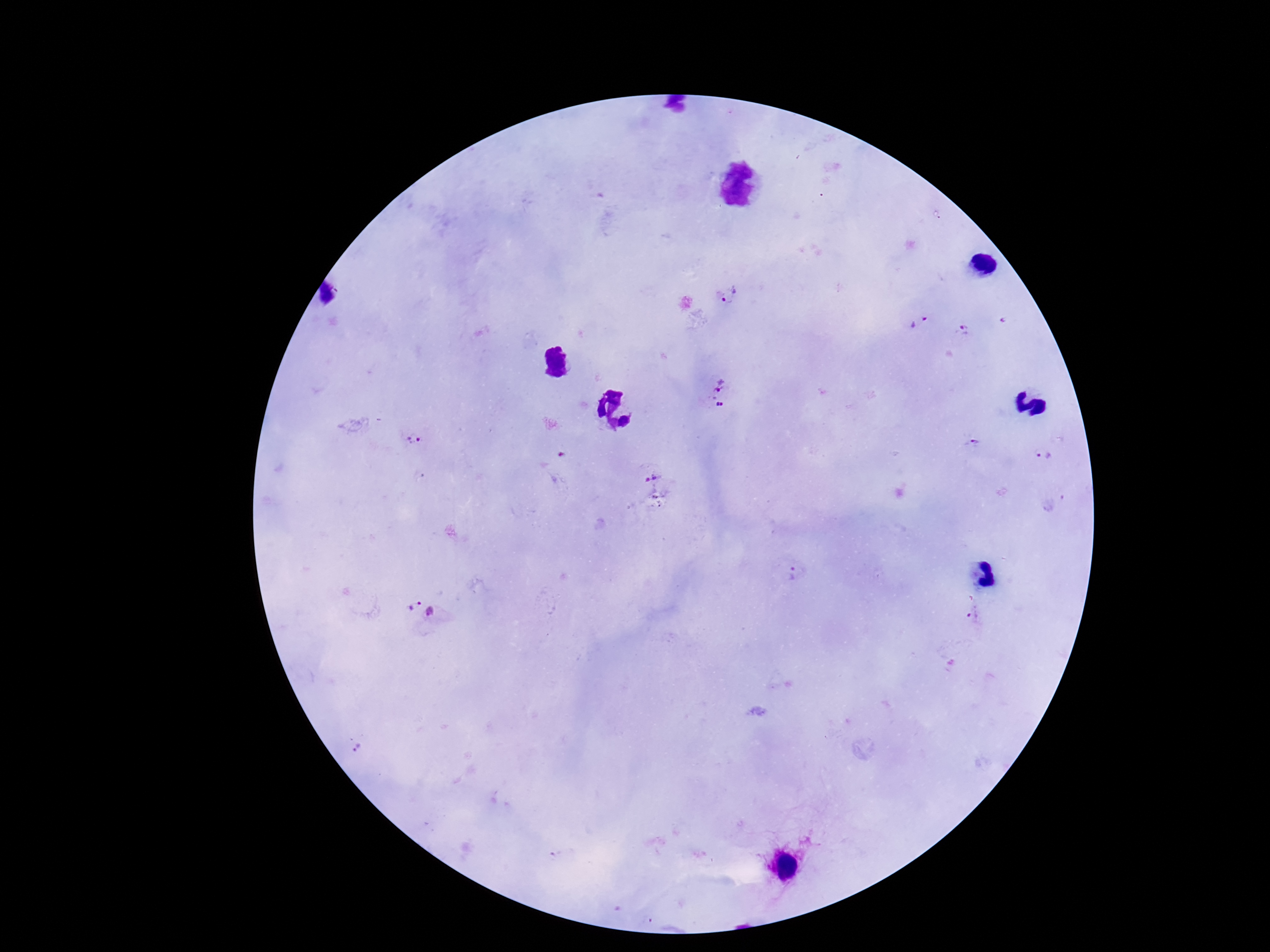

{
  "preparation": "thick peripheral-blood smear",
  "plasmodium_parasite_locations": "approximate centers as (x, y) in pixels: (730, 295), (918, 322), (964, 330), (715, 392), (412, 440), (975, 443), (1044, 456), (650, 474), (798, 574), (425, 611), (974, 612), (357, 749)",
  "capture": "smartphone camera through the microscope eyepiece",
  "field_of_view": "single",
  "magnification": "100x",
  "patient_malaria_status": "infected",
  "stain": "Giemsa",
  "image_size": "1270×952 pixels"
}